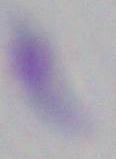
Micrograph. Captured at 1000x magnification. Toxoplasma gondii is seen.